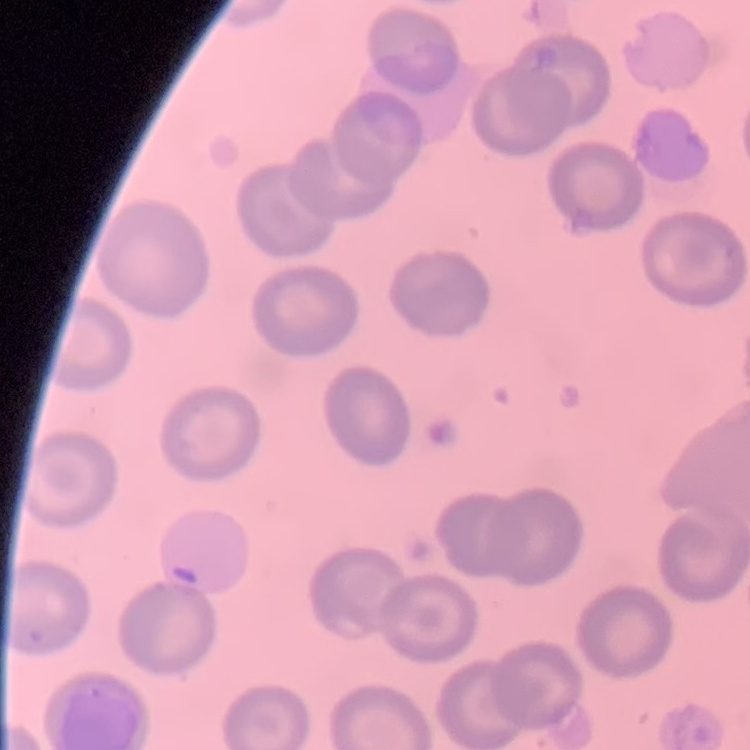
The red blood cells exhibit no rouleaux formation. Stained with either Field's or Giemsa. Square crop of a larger photomicrograph. Thin blood smear.